Report the malaria status of this cell.
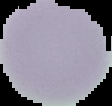

Uninfected.

Summary:
  - Image type: cell region segmented out of the field of view; surrounding area masked to black
  - Preparation: thin blood smear
  - Image size: 112×106 pixels